Classify this cell by malaria status.
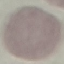

It is uninfected.

Photographed with a smartphone camera at the microscope eyepiece. Thin blood smear. Giemsa-stained preparation. Automatically extracted cell patch, resized to 64 × 64 pixels.